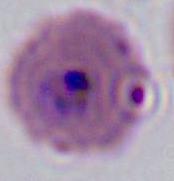 400x or 1000x magnification. Photomicrograph. A Plasmodium parasite is shown.